Give the position of every Plasmodium parasite visible.
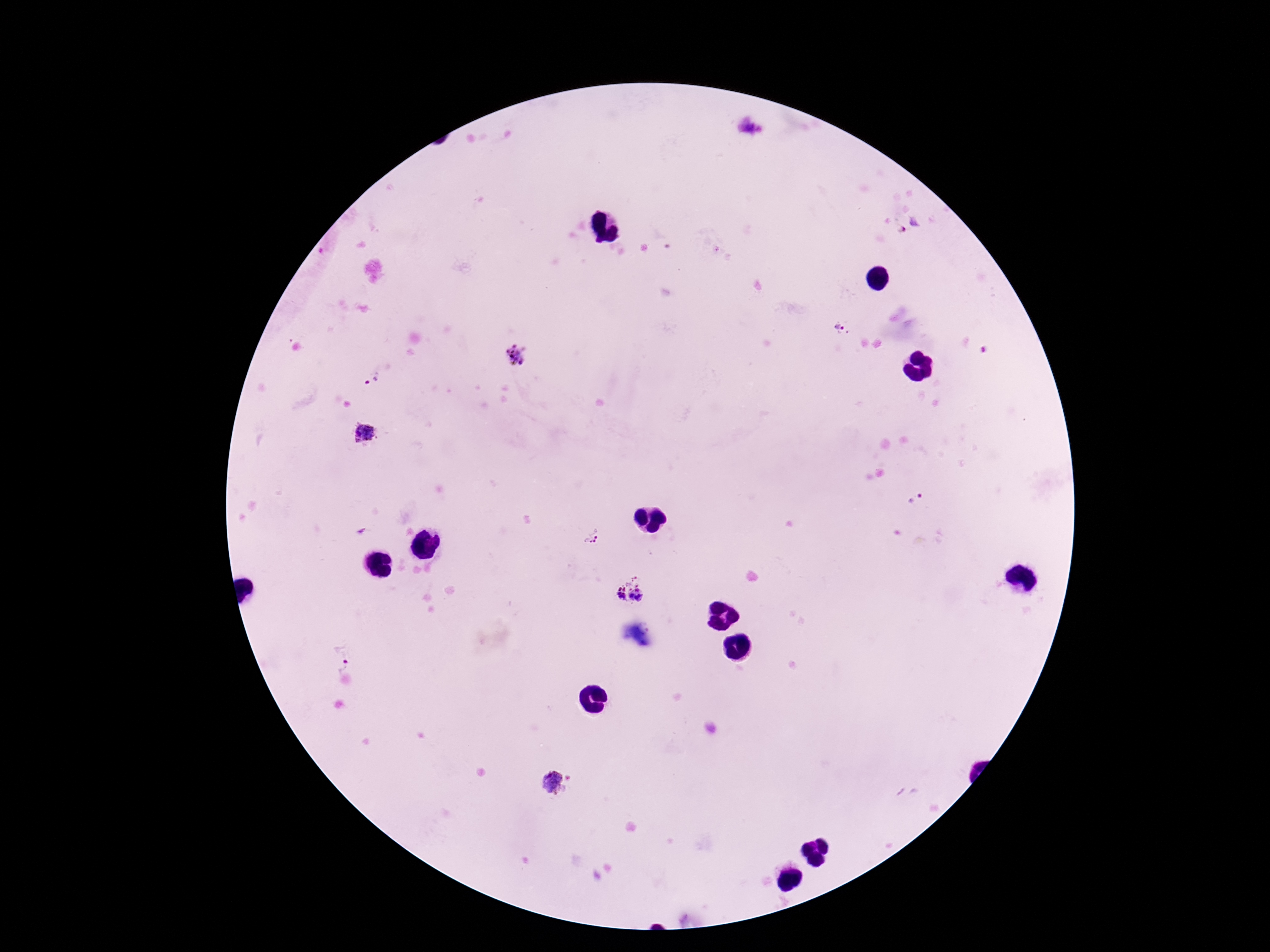
Approximate object centers, in pixels from the top-left corner.
Plasmodium parasites: (x=751, y=128), (x=910, y=226), (x=844, y=330), (x=517, y=358), (x=369, y=377), (x=364, y=434), (x=915, y=501), (x=591, y=538), (x=629, y=591), (x=340, y=659), (x=555, y=783).

Summary:
  - Preparation: thick blood film
  - Patient malaria status: infected
  - Capture: smartphone camera through the microscope eyepiece
  - Image size: 1270×952 pixels
  - Magnification: 100x
  - Stain: Giemsa
  - Field of view: one from this slide